Classify this cell by malaria status.
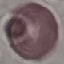
It is uninfected.

Summary:
  - Stain: Giemsa
  - Image type: automatically extracted cell patch, resized to 64 × 64 pixels
  - Capture: smartphone through the microscope eyepiece
  - Preparation: thin smear